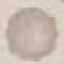
Summary:
  - Malaria status: uninfected
  - Capture: smartphone through the microscope eyepiece
  - Image type: automatically extracted cell patch, resized to 64 × 64 pixels
  - Stain: Giemsa
  - Preparation: thin blood smear